Locate every blood parasite and identify its species.
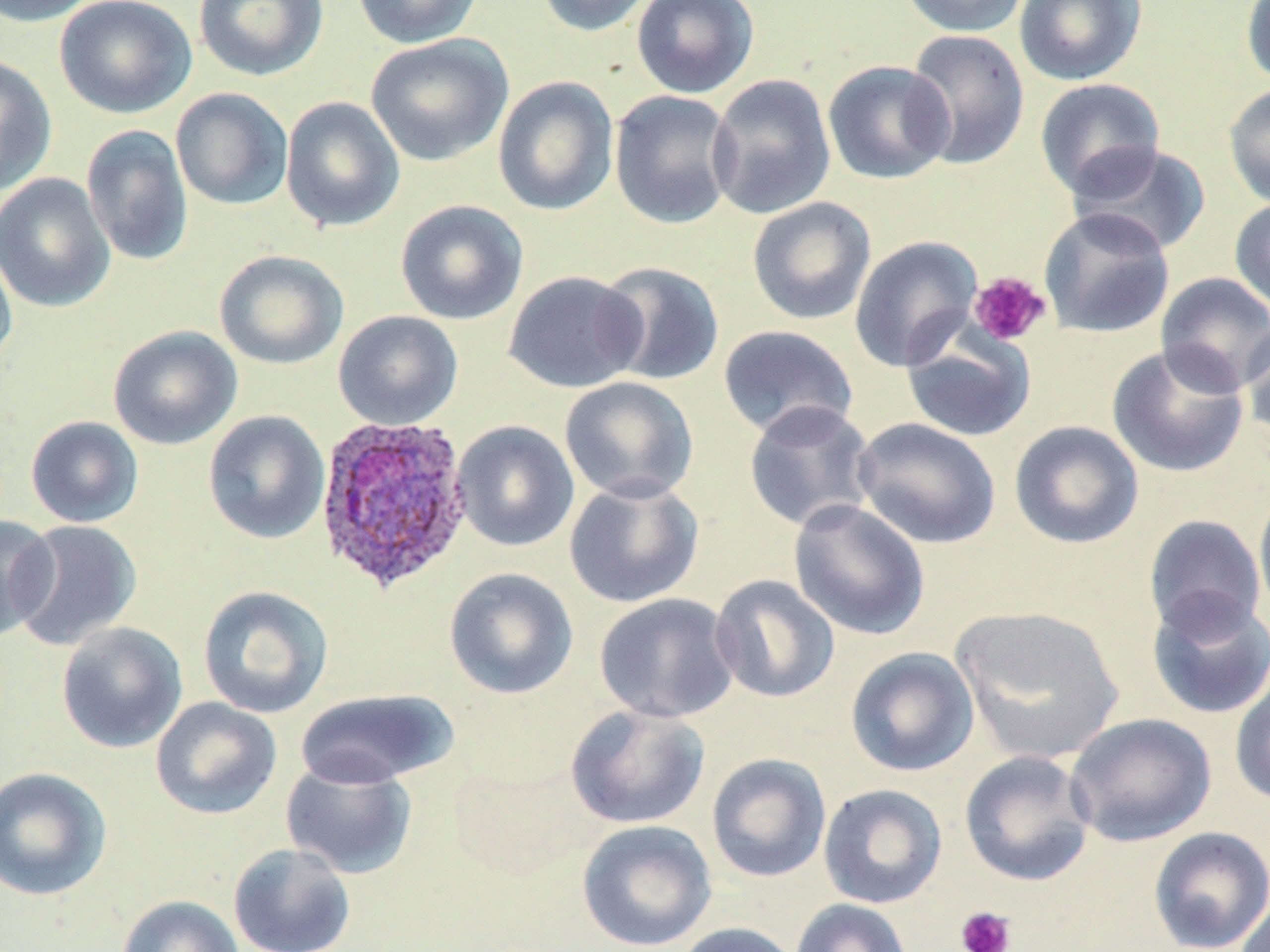
Approximate bounding boxes as (x1, y1, x2, y2) in pixels.
Plasmodium ovale-infected red blood cells: (312, 415, 475, 594).
No Plasmodium falciparum, Plasmodium malariae, Plasmodium vivax, Babesia divergens, or Trypanosoma brucei observed.

{
  "slide_level_diagnosis": "Plasmodium ovale",
  "field_of_view": "one of a larger specimen",
  "image_size": "1270×952 pixels",
  "uninfected_red_blood_cell_locations": "approximate bounding boxes as (x1, y1, x2, y2) in pixels: (54, 0, 196, 119), (194, 0, 328, 81), (352, 0, 483, 49), (536, 0, 658, 37), (631, 0, 760, 99), (898, 0, 1031, 37), (1015, 0, 1147, 86), (0, 1, 100, 27), (1240, 1, 1270, 89), (904, 29, 1030, 171), (366, 33, 513, 167), (0, 55, 57, 196), (822, 60, 955, 185), (706, 73, 836, 220), (492, 75, 619, 217), (1035, 77, 1166, 200), (1222, 82, 1270, 211), (170, 88, 294, 211), (609, 89, 740, 229), (280, 96, 405, 233), (81, 124, 194, 267), (1067, 142, 1212, 256), (0, 173, 115, 313), (747, 196, 877, 325), (1229, 197, 1270, 315), (395, 199, 528, 325), (1038, 206, 1175, 339), (849, 234, 983, 373), (0, 238, 18, 372), (214, 249, 349, 370), (595, 260, 725, 386), (502, 270, 647, 394), (1155, 272, 1270, 396), (333, 310, 463, 430), (1239, 319, 1270, 449), (717, 324, 859, 440), (108, 325, 243, 450), (901, 326, 1037, 442), (1106, 342, 1250, 478), (559, 376, 699, 503), (743, 400, 878, 533), (202, 410, 331, 545), (25, 416, 144, 528), (851, 417, 1002, 550), (452, 420, 580, 552), (1009, 420, 1144, 549), (564, 477, 704, 608), (1253, 482, 1270, 626), (788, 498, 931, 640), (0, 514, 59, 642), (1143, 514, 1266, 639), (8, 519, 142, 651), (443, 567, 578, 699), (709, 574, 840, 704), (197, 585, 334, 719), (1146, 590, 1270, 720), (594, 592, 740, 723), (950, 604, 1125, 764), (56, 621, 188, 753), (845, 647, 979, 777), (1229, 664, 1270, 807), (294, 688, 458, 789), (150, 696, 282, 820), (565, 704, 711, 829), (1064, 712, 1216, 848), (959, 750, 1097, 887), (706, 752, 831, 883), (280, 759, 418, 879), (0, 766, 112, 902), (818, 783, 948, 909), (576, 819, 717, 951), (1148, 826, 1270, 952), (227, 842, 356, 952), (116, 894, 245, 952), (1234, 894, 1270, 952), (791, 898, 913, 952), (672, 921, 802, 952)",
  "modality": "optical microscopy",
  "stain": "May-Grünwald-Giemsa",
  "magnification": "1000x",
  "platelet_locations": "approximate bounding boxes as (x1, y1, x2, y2) in pixels: (968, 271, 1051, 348), (955, 905, 1016, 952)",
  "preparation": "thin blood film"
}